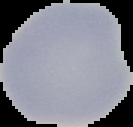

Image is 133×127 pixels. From a thin blood film. The area outside the segmented cell region is set to black. Malaria status: uninfected.